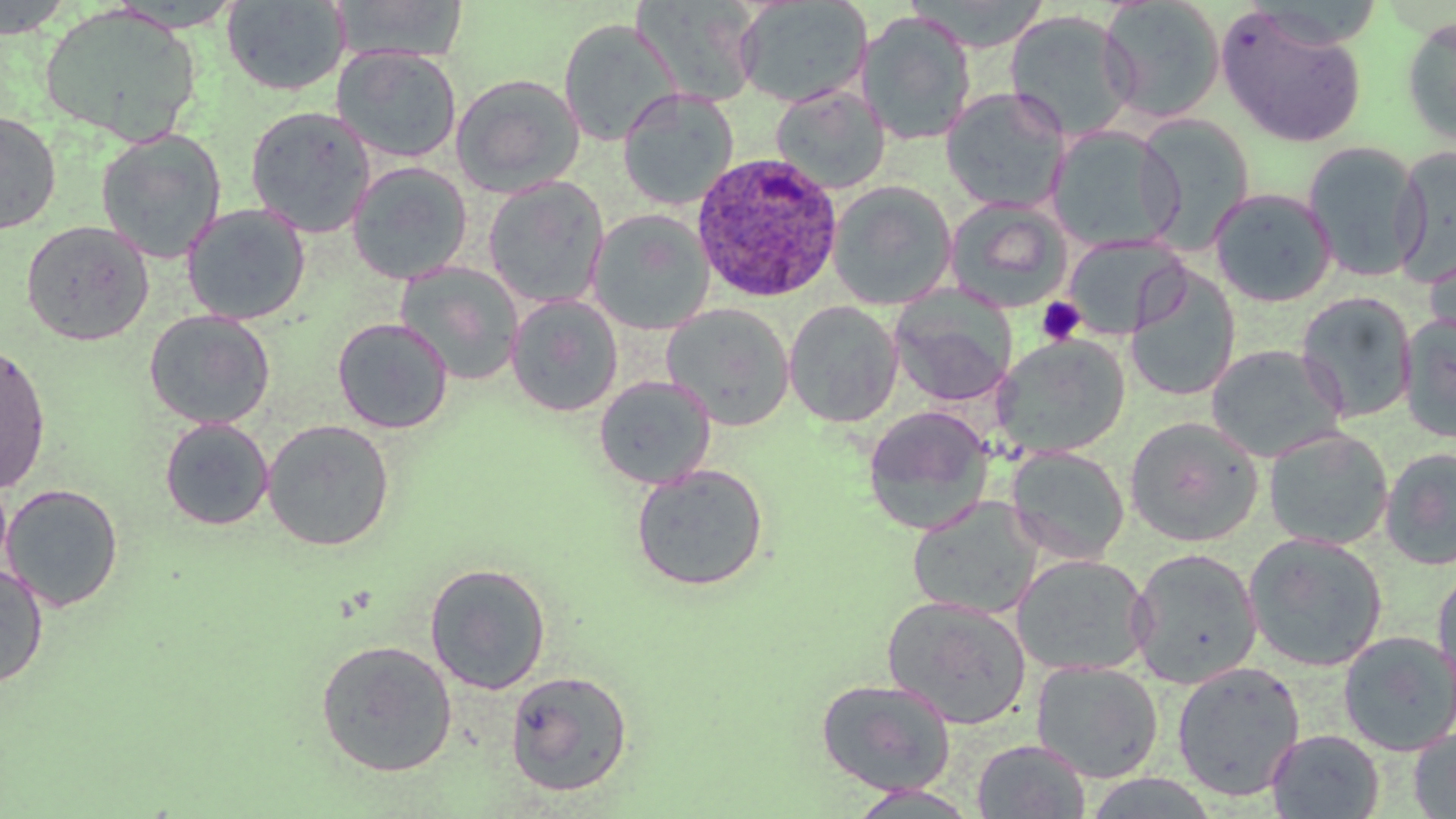

slide-level diagnosis = Plasmodium ovale
preparation = thin blood film
field of view = single
magnification = 1000x
modality = light microscopy
uninfected red blood cell locations = approximate bounding boxes as named x1/y1/x2/y2 corners in pixels: (x1=0, y1=0, x2=76, y2=39), (x1=331, y1=0, x2=469, y2=62), (x1=904, y1=0, x2=1051, y2=52), (x1=220, y1=1, x2=350, y2=96), (x1=635, y1=1, x2=763, y2=109), (x1=734, y1=1, x2=873, y2=108), (x1=1098, y1=1, x2=1227, y2=123), (x1=39, y1=3, x2=202, y2=146), (x1=1215, y1=6, x2=1369, y2=148), (x1=1003, y1=9, x2=1139, y2=143), (x1=857, y1=10, x2=977, y2=146), (x1=1399, y1=15, x2=1456, y2=149), (x1=558, y1=18, x2=678, y2=147), (x1=333, y1=45, x2=462, y2=164), (x1=450, y1=73, x2=585, y2=198), (x1=770, y1=85, x2=891, y2=194), (x1=618, y1=88, x2=739, y2=210), (x1=941, y1=88, x2=1070, y2=213), (x1=245, y1=105, x2=377, y2=237), (x1=0, y1=112, x2=61, y2=235), (x1=1133, y1=114, x2=1256, y2=251), (x1=1046, y1=125, x2=1182, y2=252), (x1=95, y1=128, x2=226, y2=264), (x1=1302, y1=141, x2=1426, y2=283), (x1=1391, y1=145, x2=1456, y2=286), (x1=347, y1=161, x2=473, y2=285), (x1=483, y1=177, x2=610, y2=309), (x1=827, y1=181, x2=957, y2=310), (x1=1209, y1=187, x2=1337, y2=307), (x1=945, y1=198, x2=1073, y2=312), (x1=182, y1=204, x2=310, y2=325), (x1=587, y1=208, x2=714, y2=334), (x1=21, y1=220, x2=153, y2=346), (x1=1062, y1=235, x2=1188, y2=339), (x1=1423, y1=242, x2=1456, y2=350), (x1=394, y1=262, x2=525, y2=386), (x1=1124, y1=268, x2=1241, y2=403), (x1=890, y1=291, x2=1017, y2=408), (x1=1295, y1=292, x2=1418, y2=423), (x1=505, y1=294, x2=623, y2=417), (x1=784, y1=301, x2=903, y2=429), (x1=661, y1=303, x2=795, y2=430), (x1=144, y1=310, x2=275, y2=430), (x1=1399, y1=313, x2=1456, y2=444), (x1=332, y1=317, x2=454, y2=434), (x1=991, y1=334, x2=1131, y2=458), (x1=0, y1=343, x2=52, y2=494), (x1=1205, y1=344, x2=1346, y2=463), (x1=593, y1=374, x2=716, y2=489), (x1=862, y1=405, x2=995, y2=535), (x1=159, y1=417, x2=274, y2=531), (x1=1125, y1=417, x2=1262, y2=546), (x1=262, y1=419, x2=395, y2=551), (x1=1264, y1=427, x2=1393, y2=550), (x1=1005, y1=445, x2=1130, y2=565), (x1=1380, y1=447, x2=1456, y2=570), (x1=630, y1=464, x2=770, y2=592), (x1=1, y1=483, x2=123, y2=612), (x1=906, y1=496, x2=1044, y2=618), (x1=1243, y1=532, x2=1389, y2=672), (x1=1128, y1=548, x2=1262, y2=688), (x1=1011, y1=553, x2=1152, y2=677), (x1=424, y1=562, x2=551, y2=694), (x1=1432, y1=562, x2=1456, y2=697), (x1=0, y1=563, x2=49, y2=689), (x1=882, y1=595, x2=1032, y2=729), (x1=1338, y1=629, x2=1456, y2=755), (x1=315, y1=639, x2=457, y2=777), (x1=1031, y1=660, x2=1164, y2=783), (x1=1170, y1=660, x2=1306, y2=801), (x1=504, y1=669, x2=633, y2=797), (x1=815, y1=678, x2=957, y2=796), (x1=1408, y1=725, x2=1456, y2=818), (x1=1265, y1=729, x2=1385, y2=818), (x1=971, y1=740, x2=1090, y2=818), (x1=1081, y1=774, x2=1221, y2=818), (x1=845, y1=785, x2=983, y2=817)
stain = May-Grünwald-Giemsa
image size = 1456×819 pixels
platelet locations = approximate bounding boxes as named x1/y1/x2/y2 corners in pixels: (x1=1036, y1=297, x2=1085, y2=346)
Plasmodium ovale-infected red blood cell locations = approximate bounding boxes as named x1/y1/x2/y2 corners in pixels: (x1=691, y1=152, x2=844, y2=302)